Look for Plasmodium parasites.
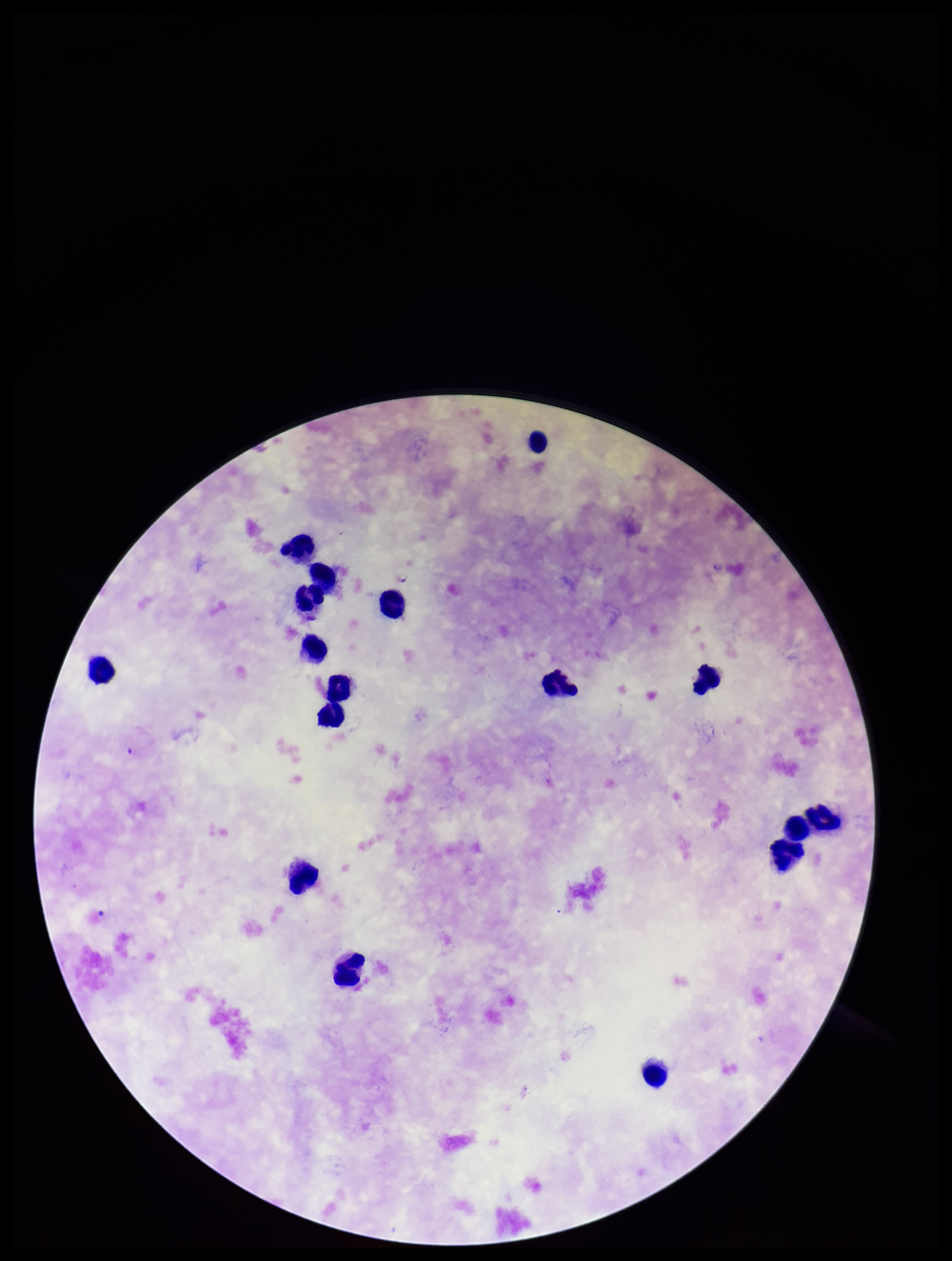
Seen.

Single field of view. Giemsa stain. Parasite count: 4. Smartphone photograph taken through the eyepiece of a microscope. Preparation: thick. Patient malaria status: positive. Image is 952×1261 pixels. Species reported for this patient: Plasmodium falciparum. Leukocyte count: 17.